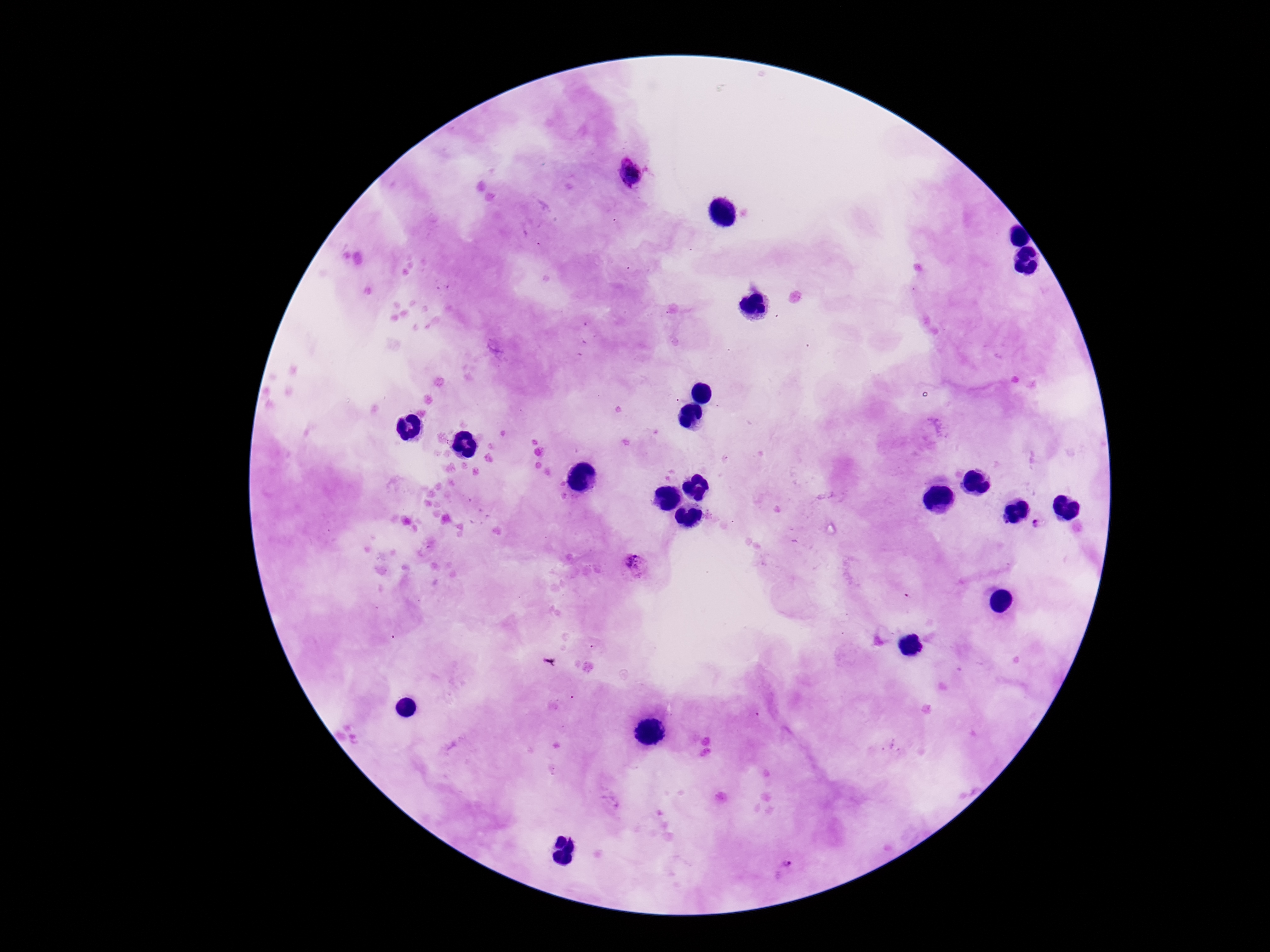
{
  "field_of_view": "one from this slide",
  "stain": "Giemsa",
  "magnification": "100x",
  "capture": "smartphone camera through the microscope eyepiece",
  "patient_malaria_status": "positive",
  "plasmodium_parasite_locations": "approximate centers as {x, y} in pixels: {630, 174}, {1000, 522}, {1038, 523}, {633, 567}, {786, 868}",
  "image_size": "1270×952 pixels",
  "preparation": "thick blood film"
}